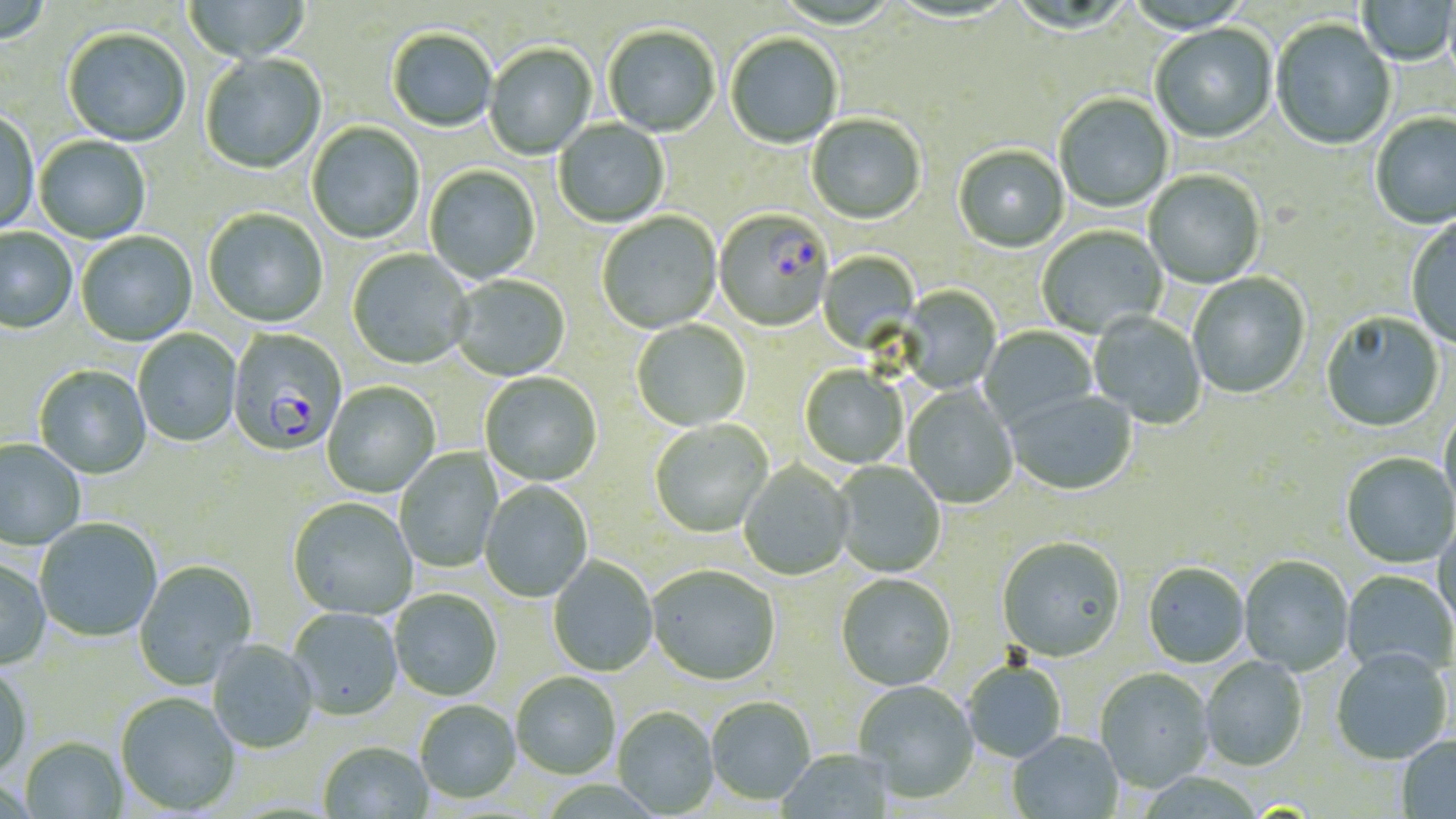

{
  "slide_level_diagnosis": "Plasmodium falciparum",
  "magnification": "1000x",
  "uninfected_red_blood_cell_locations": "approximate bounding boxes as [x1, y1, x2, y2] in pixels: [0, 0, 51, 46], [183, 1, 312, 64], [1358, 1, 1456, 67], [1271, 20, 1397, 152], [1151, 25, 1278, 145], [603, 27, 720, 138], [62, 30, 191, 148], [387, 30, 497, 133], [725, 34, 843, 150], [484, 44, 597, 161], [200, 54, 327, 176], [1055, 94, 1174, 213], [0, 112, 40, 236], [1370, 113, 1456, 231], [807, 115, 926, 226], [554, 119, 669, 228], [307, 122, 425, 245], [35, 136, 151, 244], [953, 146, 1069, 254], [425, 165, 540, 284], [1145, 171, 1266, 289], [203, 210, 328, 329], [597, 212, 722, 335], [1407, 218, 1456, 350], [1038, 226, 1168, 339], [1, 228, 77, 335], [77, 232, 197, 346], [347, 249, 474, 370], [818, 250, 920, 354], [1188, 273, 1310, 399], [451, 276, 570, 382], [897, 286, 1002, 394], [1089, 312, 1206, 429], [1321, 312, 1445, 434], [632, 320, 751, 432], [979, 326, 1098, 429], [133, 329, 241, 447], [34, 366, 151, 480], [800, 366, 907, 469], [481, 373, 602, 487], [322, 382, 440, 498], [902, 386, 1018, 509], [1004, 391, 1138, 496], [1439, 408, 1456, 519], [650, 420, 774, 538], [0, 440, 85, 551], [394, 447, 501, 573], [1341, 454, 1455, 568], [738, 461, 854, 581], [833, 461, 946, 578], [480, 482, 592, 602], [288, 498, 418, 621], [35, 519, 162, 643], [1433, 521, 1456, 641], [997, 539, 1126, 663], [547, 557, 658, 677], [1239, 557, 1353, 676], [0, 559, 51, 671], [134, 561, 257, 690], [1142, 564, 1250, 669], [646, 567, 781, 687], [1342, 571, 1455, 680], [836, 575, 956, 692], [389, 590, 502, 702], [288, 608, 403, 721], [208, 640, 319, 754], [1331, 651, 1452, 765], [1200, 657, 1307, 772], [963, 662, 1066, 763], [0, 666, 32, 781], [1095, 669, 1215, 793], [511, 674, 620, 780], [853, 681, 979, 804], [115, 693, 241, 816], [706, 698, 816, 807], [415, 701, 521, 804], [613, 707, 719, 817], [1008, 732, 1123, 818], [1396, 736, 1456, 818], [20, 738, 127, 819], [319, 742, 433, 818], [776, 749, 895, 819]",
  "stain": "May-Grünwald-Giemsa",
  "field_of_view": "one of a larger specimen",
  "modality": "optical microscopy",
  "preparation": "thin blood film",
  "image_size": "1456×819 pixels",
  "plasmodium_falciparum_infected_red_blood_cell_locations": "approximate bounding boxes as [x1, y1, x2, y2] in pixels: [714, 211, 833, 332], [227, 329, 347, 459]"
}